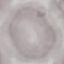 Malaria status: uninfected. Giemsa-stained preparation. Automatically extracted cell patch, resized to 64 × 64 pixels. Acquired by smartphone through the microscope eyepiece. Thin blood film.